Locate every uninfected red blood cell.
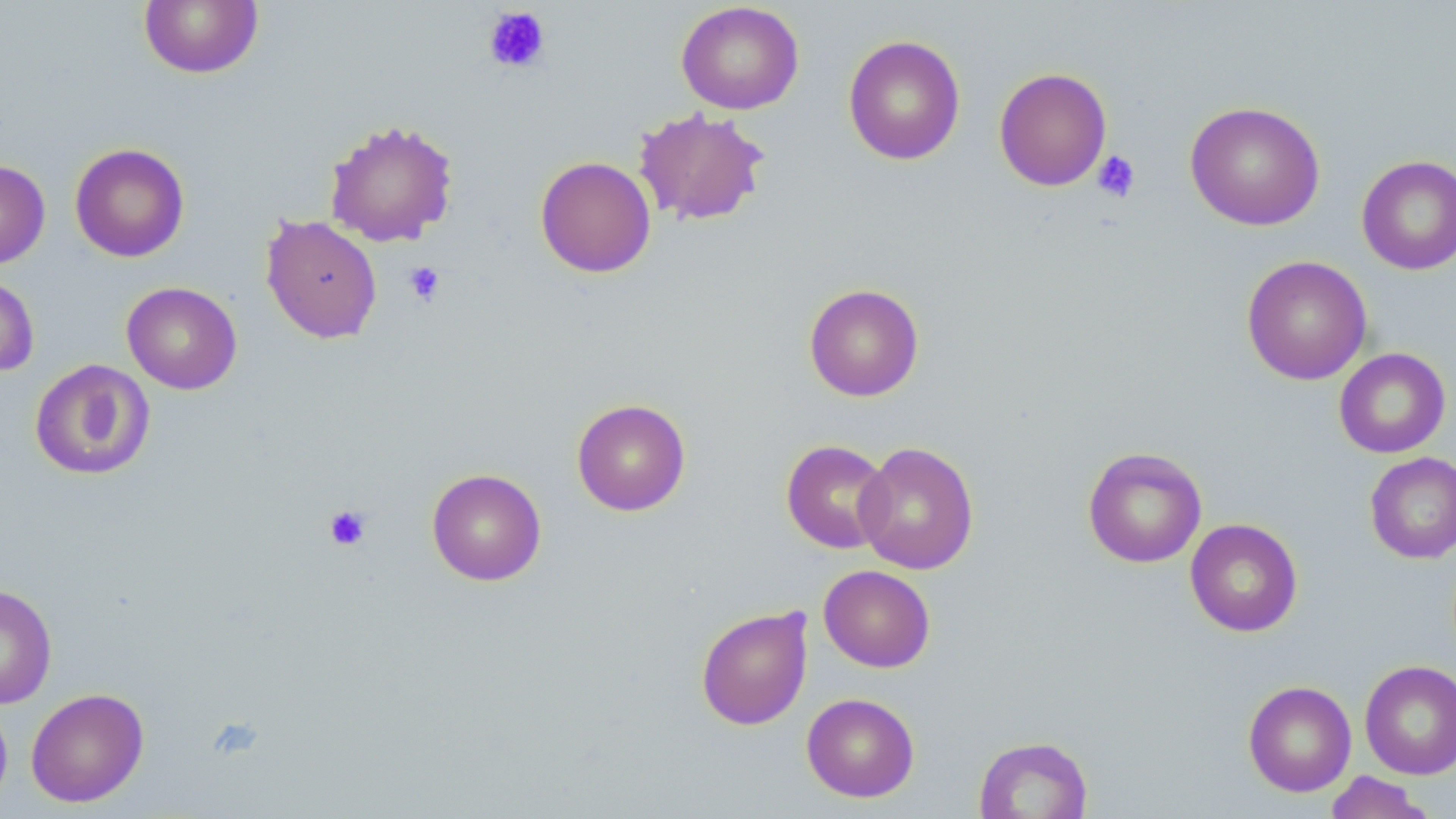
Approximate bounding boxes as (x1,y1)-(x2,y2) corner pairs in pixels.
Uninfected red blood cells: (138,0)-(263,79), (676,1)-(804,115), (842,34)-(966,166), (993,66)-(1112,191), (1184,100)-(1325,231), (634,107)-(771,227), (323,118)-(459,248), (69,142)-(190,262), (535,156)-(656,278), (1356,156)-(1455,274), (0,159)-(50,269), (260,214)-(382,344), (1241,255)-(1372,385), (0,273)-(39,378), (122,281)-(242,394), (804,283)-(924,402), (1334,348)-(1451,458), (29,359)-(156,481), (571,398)-(691,516), (781,439)-(893,554), (854,441)-(979,575), (1082,446)-(1207,568), (1364,452)-(1456,563), (426,468)-(547,586), (1185,518)-(1303,637), (819,565)-(936,672), (0,583)-(57,709), (695,605)-(813,731), (1359,660)-(1456,780), (1243,680)-(1357,797), (25,687)-(149,807), (801,692)-(920,802), (0,696)-(12,814), (973,736)-(1093,818), (1324,771)-(1436,819).

Summary:
  - Platelet locations: (483,7)-(551,74), (1092,150)-(1141,202), (404,261)-(446,305), (323,504)-(372,551)
  - Slide-level diagnosis: negative for blood parasites
  - Field of view: one of a larger specimen
  - Stain: May-Grünwald-Giemsa
  - Modality: optical microscopy
  - Image size: 1456×819 pixels
  - Magnification: 1000x
  - Preparation: thin blood film